Comment on the morphology of the erythrocytes.
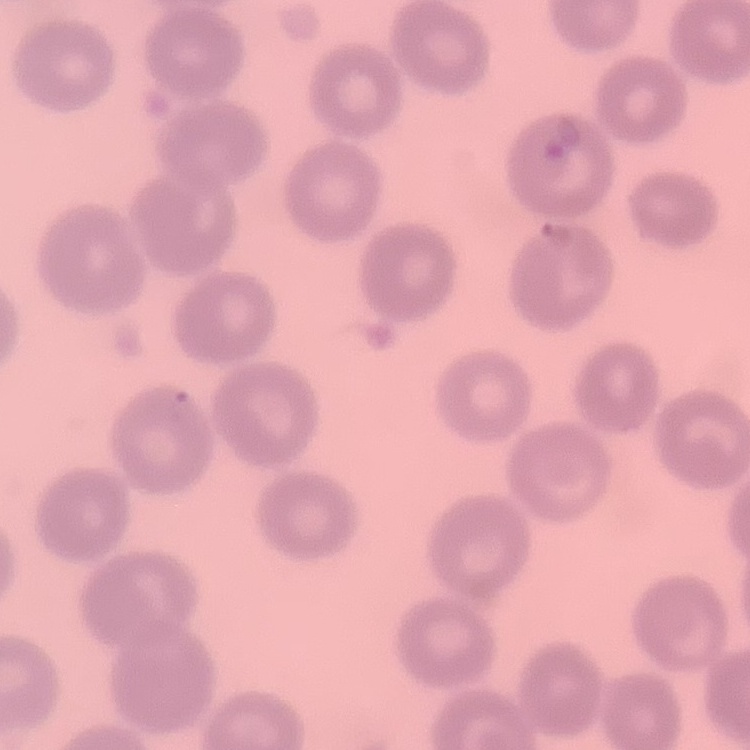

No rouleaux formation.

Summary:
  - Image type: one tile cut from a larger photomicrograph
  - Preparation: thin blood smear
  - Stain: Field's or Giemsa